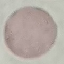

Malaria status: uninfected. Giemsa-stained preparation. Thin blood smear. Acquired by smartphone through the microscope eyepiece. Automatically extracted cell patch, resized to 64 × 64 pixels.